Locate every blood parasite and identify its species.
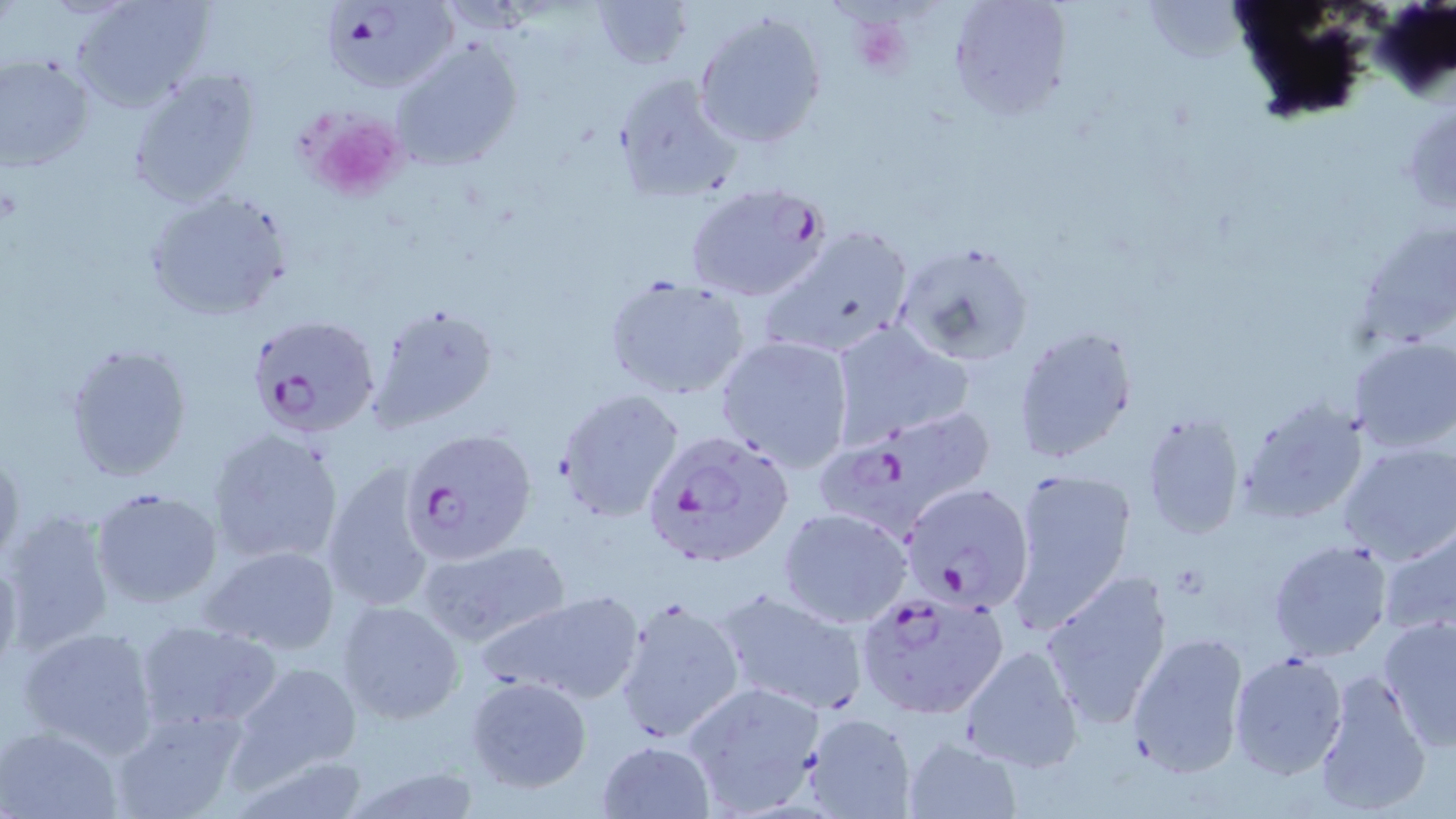

Approximate bounding boxes as (x1,y1)-(x2,y2) corner pairs in pixels.
Plasmodium falciparum-infected red blood cells: (323,3)-(457,95), (684,180)-(832,303), (248,313)-(382,440), (814,409)-(994,535), (401,427)-(537,565), (643,428)-(796,571), (899,482)-(1036,612), (855,587)-(1010,720).
No Plasmodium ovale, Plasmodium malariae, Plasmodium vivax, Babesia divergens, or Trypanosoma brucei observed.

slide-level diagnosis = Plasmodium falciparum
platelet locations = approximate bounding boxes as (x1,y1)-(x2,y2) corner pairs in pixels: (855,19)-(914,79), (305,109)-(408,202)
image size = 1456×819 pixels
uninfected red blood cell locations = approximate bounding boxes as (x1,y1)-(x2,y2) corner pairs in pixels: (71,0)-(213,110), (587,0)-(693,70), (947,0)-(1072,121), (691,10)-(829,152), (392,38)-(525,172), (0,55)-(96,172), (125,69)-(264,209), (612,73)-(742,204), (143,189)-(295,323), (761,225)-(917,360), (895,241)-(1035,368), (603,274)-(751,401), (367,303)-(501,433), (828,323)-(972,443), (1012,324)-(1139,464), (714,335)-(856,472), (1347,337)-(1456,453), (65,340)-(192,481), (554,389)-(684,524), (1236,396)-(1369,526), (1139,412)-(1246,540), (207,427)-(344,568), (1338,442)-(1456,565), (0,443)-(22,565), (322,461)-(438,613), (1004,466)-(1140,627), (90,488)-(223,610), (777,507)-(913,628), (1,508)-(117,654), (1377,524)-(1456,642), (416,538)-(571,648), (1268,538)-(1393,662), (204,545)-(342,655), (0,548)-(24,680), (1038,568)-(1175,731), (714,587)-(869,716), (475,590)-(648,706), (613,594)-(748,746), (335,599)-(465,724), (1377,615)-(1456,752), (133,619)-(280,732), (17,625)-(161,756), (1126,631)-(1251,778), (958,643)-(1085,774), (1227,650)-(1349,781), (226,660)-(364,787), (1312,668)-(1433,816), (465,675)-(592,794), (681,677)-(825,818), (110,707)-(247,819), (803,713)-(917,819), (0,724)-(123,819), (903,736)-(1022,818), (596,740)-(716,819), (223,756)-(379,818), (339,763)-(488,819)
preparation = thin blood film
modality = light microscopy
magnification = 1000x
field of view = one of a larger specimen
stain = May-Grünwald-Giemsa